Mark where leukocytes are.
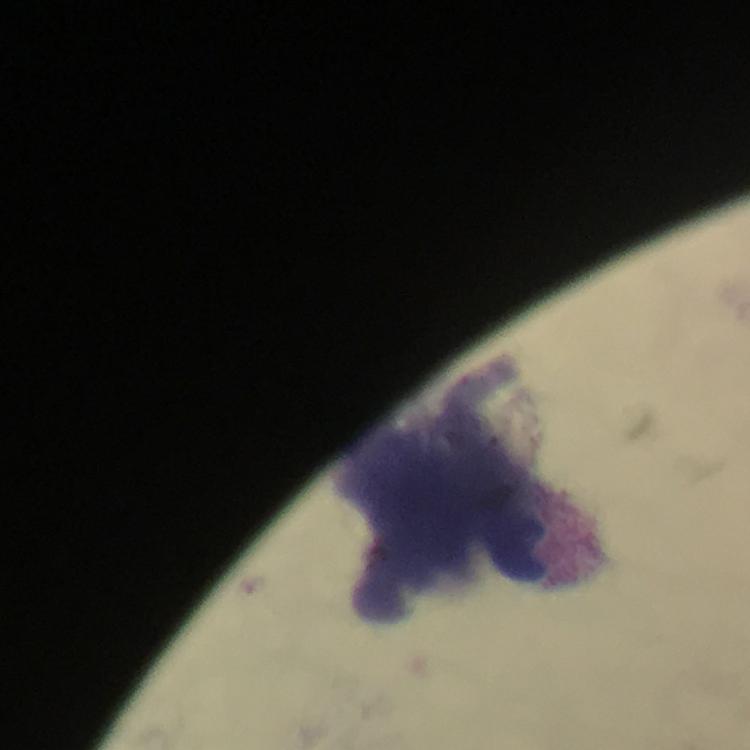
Approximate object centers, in pixels from the top-left corner.
Leukocytes: (x=444, y=523).

Summary:
  - Immersion oil: used
  - Image size: 750×750 pixels
  - Preparation: thick smear
  - Malaria parasites: none seen
  - Stain: Giemsa
  - Capture: smartphone mounted on the microscope
  - Magnification: 100x
  - Cropped from: one field of view
  - Context: from a malaria diagnostic workup